State which cell type is depicted.
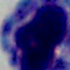
A leukocyte.

modality = photomicrograph
magnification = 1000x